Outline platelets.
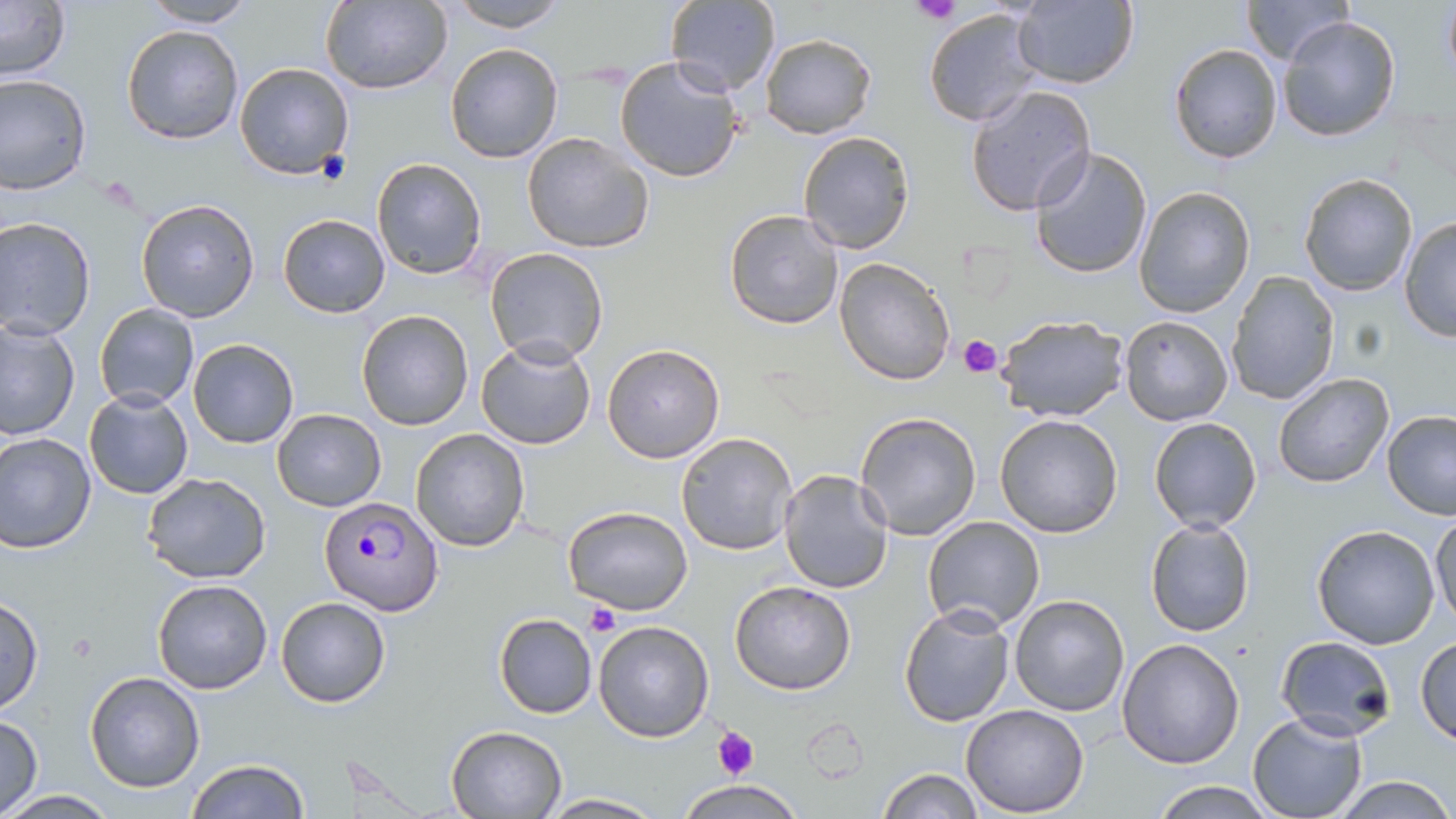

Approximate bounding boxes as (x1, y1, x2, y2) in pixels.
Platelets: (911, 0, 963, 26), (316, 149, 350, 186), (958, 334, 1003, 379), (585, 603, 622, 637), (712, 728, 759, 780).

Summary:
  - Plasmodium falciparum-infected red blood cell locations: (320, 495, 445, 615)
  - Uninfected red blood cell locations: (320, 0, 452, 94), (449, 0, 567, 31), (666, 0, 781, 98), (1009, 1, 1140, 89), (1239, 1, 1350, 65), (1440, 1, 1456, 83), (0, 2, 71, 82), (140, 2, 257, 28), (922, 7, 1044, 127), (1277, 13, 1401, 142), (121, 24, 244, 144), (759, 33, 876, 137), (444, 43, 564, 164), (1169, 43, 1284, 165), (613, 55, 745, 185), (233, 61, 353, 180), (0, 72, 93, 193), (965, 84, 1096, 215), (521, 130, 654, 256), (797, 131, 914, 254), (1028, 145, 1153, 281), (371, 157, 486, 279), (1298, 172, 1418, 296), (1134, 186, 1256, 318), (134, 197, 260, 321), (723, 208, 847, 329), (277, 213, 390, 317), (1398, 216, 1456, 342), (0, 217, 97, 340), (483, 247, 610, 367), (833, 257, 956, 386), (1226, 272, 1340, 407), (94, 303, 199, 411), (356, 311, 473, 430), (993, 313, 1130, 423), (1119, 314, 1233, 425), (0, 320, 79, 441), (476, 336, 598, 452), (188, 338, 300, 449), (602, 344, 725, 463), (1272, 372, 1396, 490), (82, 388, 194, 500), (270, 408, 387, 511), (854, 410, 983, 540), (1381, 410, 1456, 520), (995, 414, 1125, 539), (1148, 416, 1263, 534), (410, 427, 529, 551), (676, 431, 798, 556), (0, 432, 97, 553), (777, 468, 893, 596), (141, 472, 271, 584), (563, 506, 693, 616), (1430, 511, 1455, 631), (922, 515, 1046, 633), (1144, 517, 1255, 637), (1311, 524, 1440, 649), (152, 578, 273, 694), (729, 581, 857, 695), (1008, 594, 1130, 717), (0, 595, 43, 715), (275, 597, 391, 708), (898, 602, 1016, 727), (494, 614, 598, 718), (593, 620, 714, 742), (1416, 634, 1456, 743), (1274, 636, 1397, 741), (1116, 638, 1245, 770), (83, 671, 206, 793), (960, 704, 1090, 817), (1246, 713, 1366, 819), (1, 715, 43, 815), (444, 725, 567, 818), (185, 758, 311, 819), (877, 769, 984, 818), (1334, 775, 1455, 818), (674, 779, 806, 817), (1147, 779, 1281, 818), (4, 790, 118, 819), (541, 792, 664, 818)
  - Slide-level diagnosis: Plasmodium falciparum
  - Modality: optical microscopy
  - Stain: May-Grünwald-Giemsa
  - Preparation: thin blood film
  - Magnification: 1000x
  - Field of view: one of a larger specimen
  - Image size: 1456×819 pixels